State which parasite is depicted.
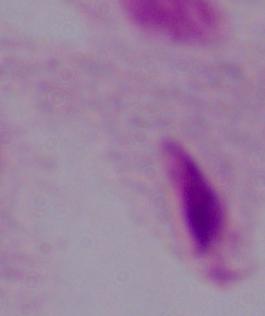

A trichomonad.

Summary:
  - Modality: micrograph
  - Magnification: 1000x